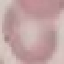

Summary:
  - Malaria status: uninfected
  - Image type: automatically extracted cell patch, resized to 64 × 64 pixels
  - Capture: smartphone camera at the microscope eyepiece
  - Stain: Giemsa
  - Preparation: thin smear